Name the parasite shown.
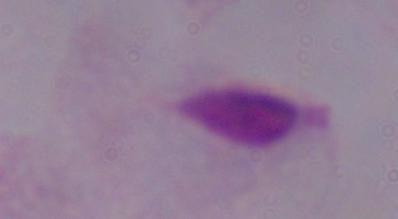

This is a trichomonad.

magnification: 1000x
modality: micrograph